Comment on the morphology of the erythrocytes.
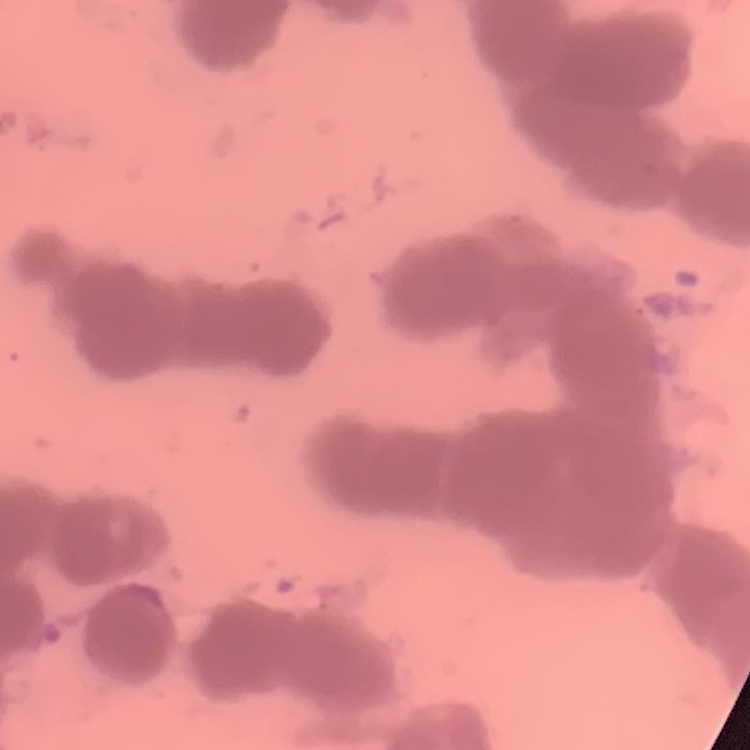

They show rouleaux formation.

Square crop of a larger photomicrograph. Thin peripheral smear. Field's or Giemsa stain.